Give the extent of all Plasmodium falciparum-infected red blood cells.
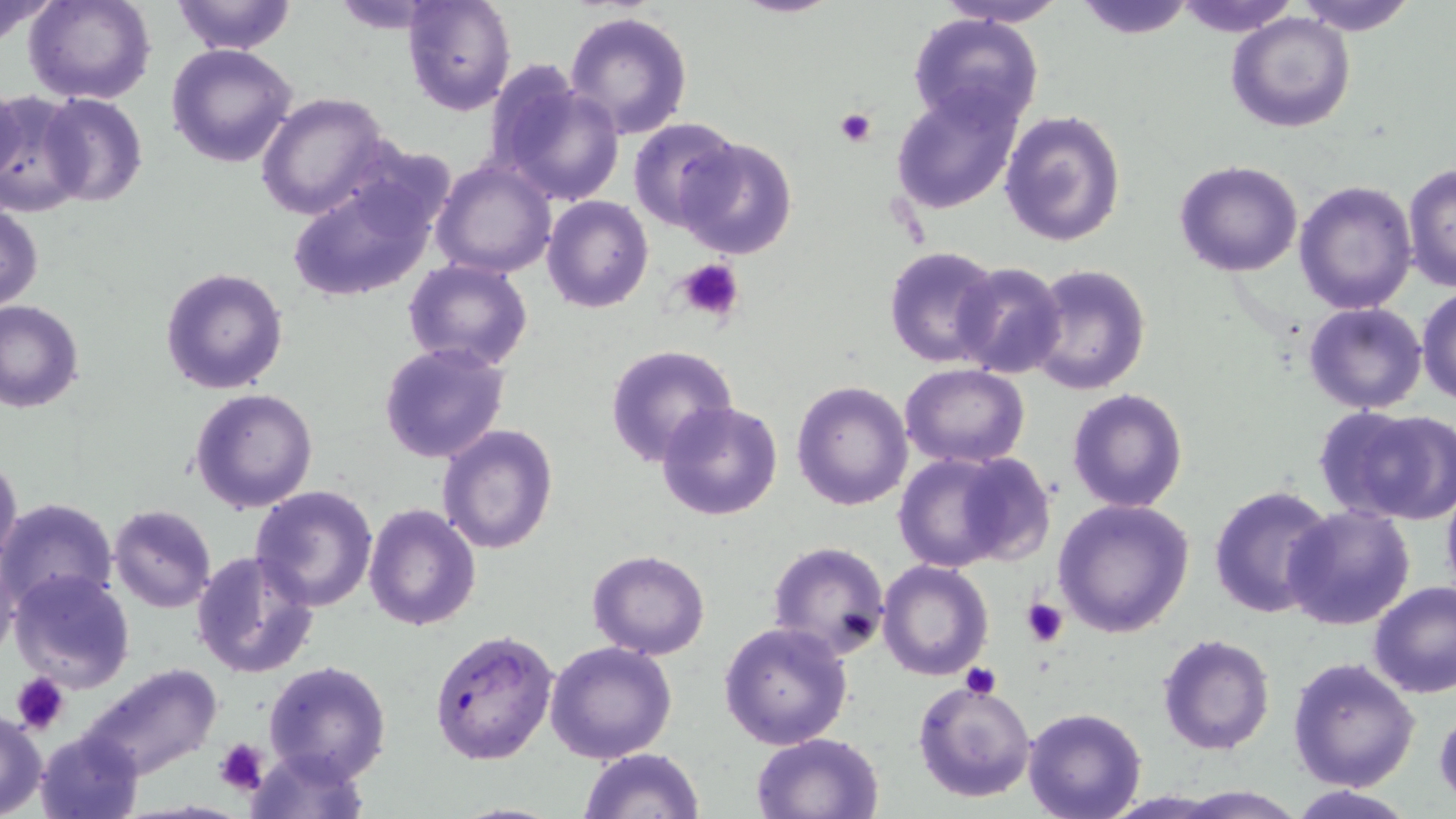

Approximate bounding boxes as named x1/y1/x2/y2 corners in pixels.
Plasmodium falciparum-infected red blood cells: (x1=429, y1=630, x2=559, y2=765).

Summary:
  - Uninfected red blood cell locations: (x1=0, y1=0, x2=61, y2=45), (x1=25, y1=0, x2=155, y2=104), (x1=169, y1=0, x2=297, y2=54), (x1=403, y1=0, x2=517, y2=115), (x1=933, y1=0, x2=1070, y2=27), (x1=1072, y1=0, x2=1199, y2=39), (x1=1175, y1=0, x2=1299, y2=36), (x1=1292, y1=0, x2=1420, y2=36), (x1=563, y1=10, x2=693, y2=140), (x1=1226, y1=11, x2=1357, y2=133), (x1=907, y1=13, x2=1044, y2=133), (x1=166, y1=43, x2=298, y2=169), (x1=491, y1=73, x2=626, y2=207), (x1=0, y1=83, x2=26, y2=198), (x1=889, y1=83, x2=1024, y2=213), (x1=0, y1=92, x2=87, y2=214), (x1=37, y1=92, x2=149, y2=208), (x1=256, y1=92, x2=390, y2=221), (x1=999, y1=109, x2=1127, y2=249), (x1=627, y1=118, x2=744, y2=232), (x1=674, y1=136, x2=798, y2=260), (x1=431, y1=158, x2=558, y2=279), (x1=1174, y1=159, x2=1303, y2=278), (x1=1402, y1=162, x2=1456, y2=294), (x1=288, y1=170, x2=443, y2=305), (x1=1294, y1=181, x2=1418, y2=317), (x1=541, y1=195, x2=653, y2=313), (x1=1, y1=201, x2=44, y2=311), (x1=884, y1=245, x2=1004, y2=367), (x1=402, y1=260, x2=534, y2=372), (x1=951, y1=262, x2=1066, y2=381), (x1=1024, y1=262, x2=1151, y2=397), (x1=159, y1=265, x2=290, y2=394), (x1=1416, y1=286, x2=1456, y2=405), (x1=0, y1=299, x2=85, y2=413), (x1=1303, y1=301, x2=1429, y2=416), (x1=378, y1=341, x2=510, y2=463), (x1=603, y1=344, x2=739, y2=465), (x1=900, y1=363, x2=1029, y2=467), (x1=790, y1=380, x2=913, y2=510), (x1=189, y1=388, x2=319, y2=515), (x1=1067, y1=388, x2=1189, y2=513), (x1=655, y1=399, x2=784, y2=520), (x1=1315, y1=404, x2=1456, y2=526), (x1=437, y1=425, x2=561, y2=555), (x1=890, y1=448, x2=1047, y2=573), (x1=0, y1=454, x2=23, y2=569), (x1=1440, y1=477, x2=1456, y2=603), (x1=1208, y1=482, x2=1337, y2=620), (x1=249, y1=484, x2=379, y2=611), (x1=1052, y1=497, x2=1193, y2=637), (x1=2, y1=498, x2=118, y2=611), (x1=363, y1=502, x2=482, y2=631), (x1=107, y1=505, x2=217, y2=613), (x1=1283, y1=506, x2=1415, y2=630), (x1=765, y1=540, x2=891, y2=659), (x1=1, y1=544, x2=22, y2=665), (x1=192, y1=550, x2=320, y2=680), (x1=586, y1=550, x2=711, y2=660), (x1=877, y1=559, x2=994, y2=681), (x1=7, y1=567, x2=136, y2=694), (x1=1367, y1=580, x2=1456, y2=698), (x1=718, y1=621, x2=854, y2=749), (x1=1156, y1=633, x2=1275, y2=754), (x1=544, y1=641, x2=678, y2=765), (x1=1288, y1=657, x2=1419, y2=792), (x1=263, y1=661, x2=392, y2=784), (x1=79, y1=662, x2=222, y2=781), (x1=914, y1=678, x2=1036, y2=804), (x1=1433, y1=702, x2=1456, y2=805), (x1=1022, y1=706, x2=1147, y2=819), (x1=0, y1=708, x2=48, y2=817), (x1=34, y1=729, x2=144, y2=818), (x1=751, y1=731, x2=884, y2=818), (x1=243, y1=745, x2=369, y2=819), (x1=577, y1=748, x2=705, y2=819), (x1=1284, y1=785, x2=1422, y2=818)
  - Platelet locations: (x1=835, y1=108, x2=876, y2=149), (x1=670, y1=257, x2=744, y2=322), (x1=1020, y1=596, x2=1068, y2=645), (x1=958, y1=663, x2=1002, y2=700), (x1=11, y1=672, x2=69, y2=733), (x1=213, y1=737, x2=269, y2=793)
  - Slide-level diagnosis: Plasmodium falciparum
  - Stain: May-Grünwald-Giemsa
  - Modality: optical microscopy
  - Preparation: thin blood smear
  - Magnification: 1000x
  - Image size: 1456×819 pixels
  - Field of view: one of a larger specimen